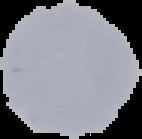
{
  "image_type": "segmented cell region with the area outside set to black",
  "malaria_status": "uninfected",
  "image_size": "142×139 pixels",
  "preparation": "thin blood film"
}